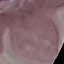

Summary:
  - Malaria status: uninfected
  - Image type: cell patch, automatically extracted from a larger field of view and resized to 64 × 64 pixels
  - Preparation: thin blood film
  - Stain: Giemsa
  - Capture: smartphone through the microscope eyepiece